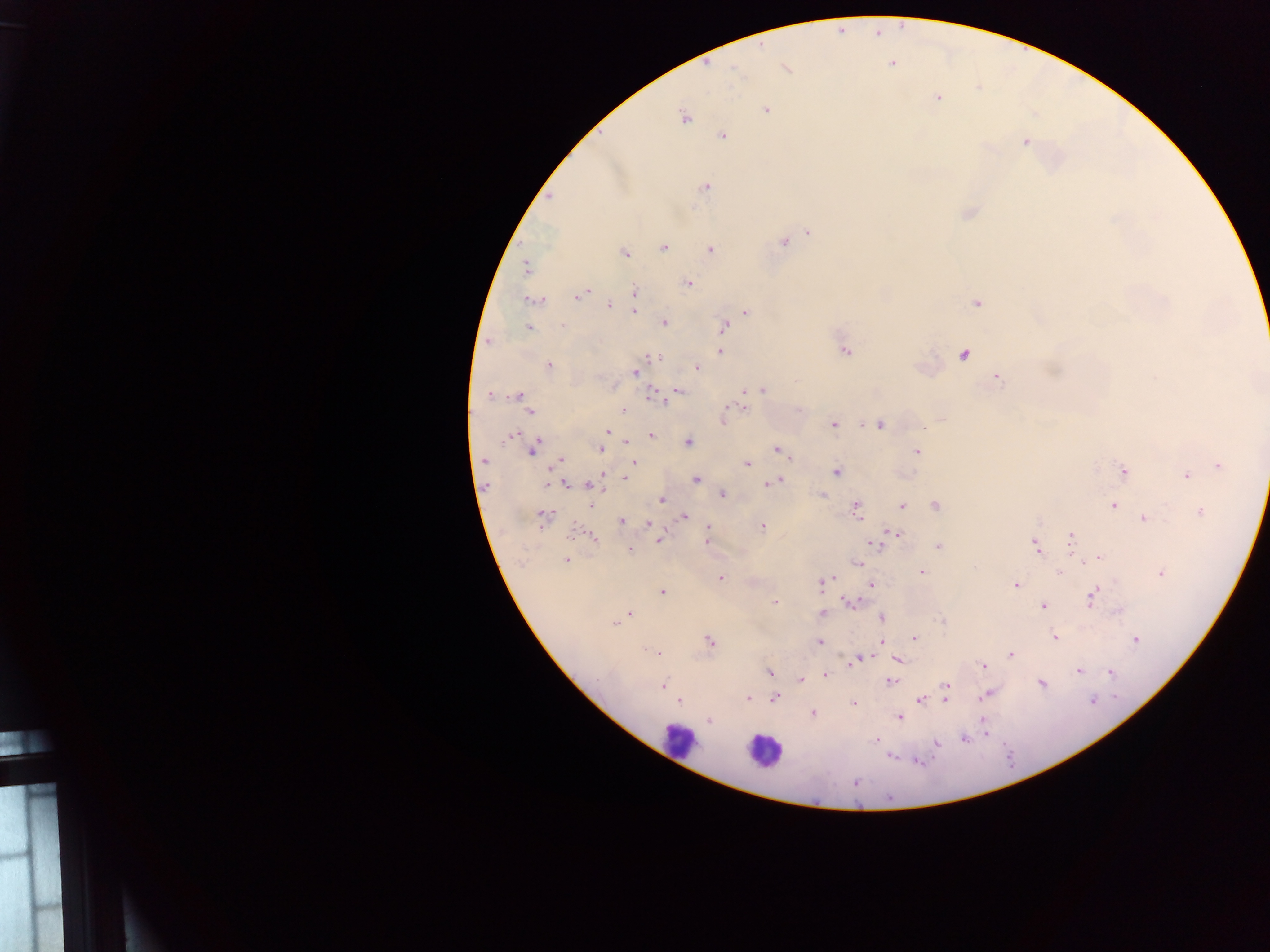 Approximate centers as (x, y) in pixels. Malaria parasite locations: (877, 33), (891, 63), (785, 68), (937, 98), (765, 109), (683, 117), (722, 135), (1025, 141), (705, 187), (551, 196), (967, 213), (808, 231), (784, 241), (662, 248), (709, 249), (623, 253), (525, 267), (687, 283), (634, 290), (578, 295), (533, 301), (976, 303), (609, 305), (633, 311), (744, 311), (664, 322), (561, 325), (723, 326), (527, 327), (489, 341), (719, 351), (845, 351), (964, 353), (659, 358), (548, 366), (696, 367), (635, 372), (996, 376), (762, 389), (677, 390), (743, 391), (654, 394), (489, 395), (518, 396), (522, 400), (743, 407), (528, 411), (623, 411), (726, 411), (941, 418), (722, 422), (833, 424), (879, 424), (606, 431), (512, 434), (650, 434), (626, 442), (688, 442), (532, 447), (600, 448), (777, 449), (916, 451), (484, 460), (559, 460), (633, 462), (746, 463), (1218, 465), (836, 471), (1122, 471), (603, 473), (1186, 474), (625, 478), (696, 479), (776, 481), (550, 483), (565, 483), (591, 485), (721, 494), (821, 495), (661, 499), (591, 504), (901, 505), (935, 505), (1113, 505), (855, 509), (1201, 511), (683, 516), (542, 518), (1144, 518), (622, 521), (648, 522), (762, 526), (708, 528), (897, 533), (591, 537), (1071, 538), (659, 539), (708, 540), (870, 544), (938, 546), (1036, 546), (629, 549), (1098, 557), (567, 560), (857, 564), (921, 572), (1059, 573), (1161, 573), (720, 577), (821, 582), (871, 583), (1015, 585), (662, 591), (1093, 597), (774, 602), (849, 602), (1043, 606), (630, 613), (822, 614), (881, 618), (619, 619), (615, 623), (1053, 637), (914, 638), (1135, 638), (882, 641), (709, 642), (820, 642), (655, 652), (1010, 654), (857, 658), (896, 660), (983, 665), (1078, 671), (1109, 671), (769, 672), (825, 676), (800, 680), (891, 680), (1041, 683), (662, 684), (946, 686), (986, 694), (748, 698), (773, 698), (920, 698), (945, 698), (679, 701), (853, 703), (812, 712), (900, 716), (710, 719), (982, 720), (984, 734), (963, 738), (875, 740), (935, 743), (889, 756), (916, 760), (855, 781). Leukocyte locations: (679, 741), (764, 751). Image is 1270×952 pixels. Photographed through a microscope with a mobile-phone camera. Sample from Ghana. One field of view. Thick blood smear.